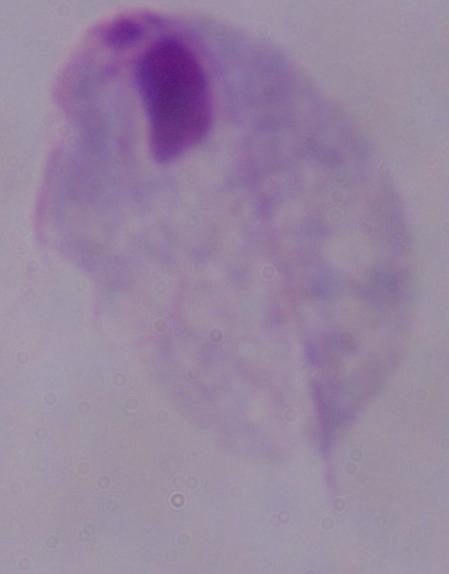

1000x magnification. Photomicrograph. A trichomonad is shown.